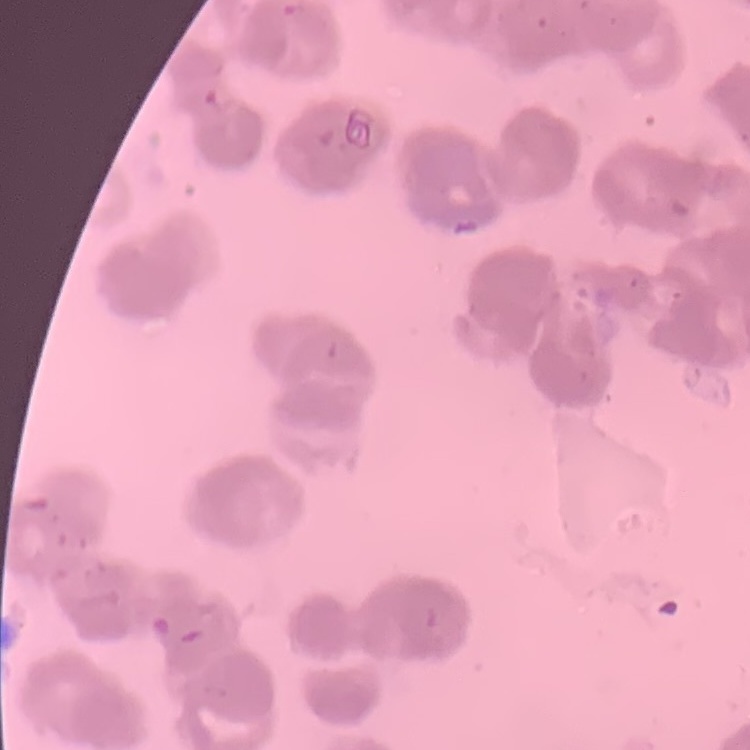

Summary:
  - Erythrocyte morphology: rouleaux formation
  - Stain: Field's or Giemsa
  - Preparation: thin blood smear
  - Image type: square crop of a larger photomicrograph